Assess this cell for malaria.
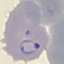
It is parasitized.

image type = cell patch, automatically extracted from a larger field of view and resized to 64 × 64 pixels
capture = smartphone through the microscope eyepiece
preparation = thin blood smear
stain = Giemsa